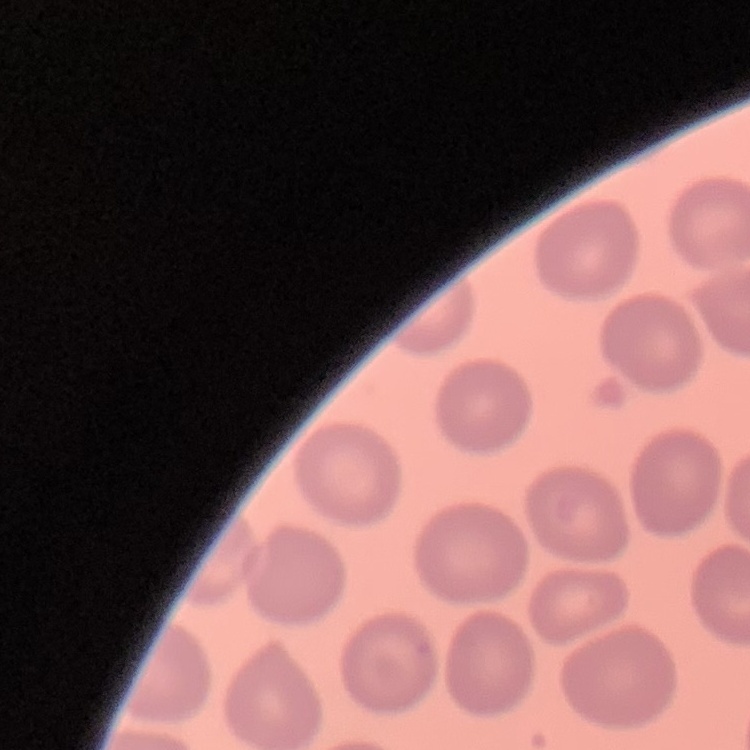

Summary:
  - Erythrocyte morphology: no rouleaux formation
  - Stain: Field's or Giemsa
  - Preparation: thin peripheral smear
  - Image type: one tile cut from a larger photomicrograph